Name the blood parasite species.
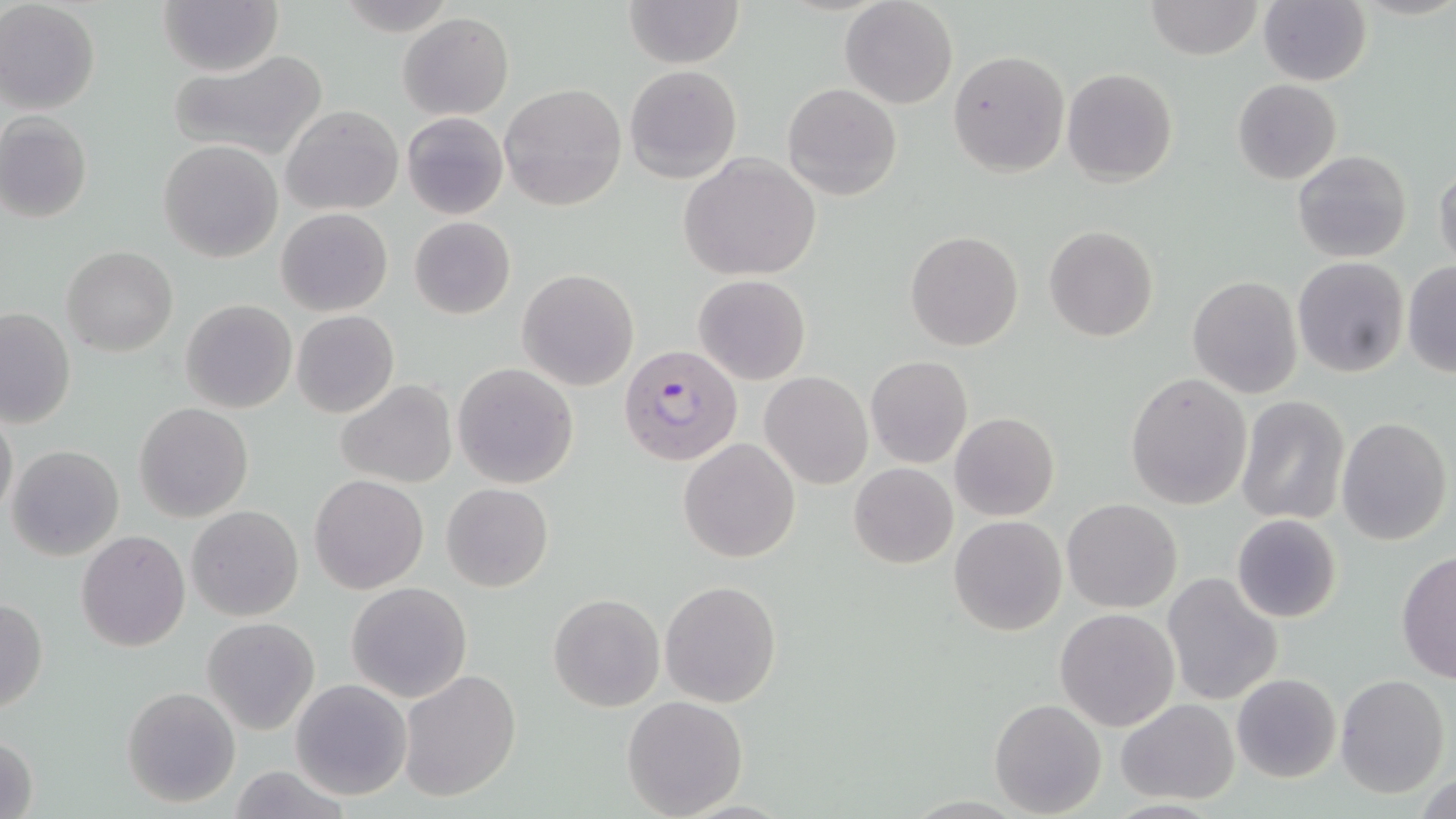
Plasmodium falciparum.

Summary:
  - Coordinate format: approximate bounding boxes as (x1,y1)-(x2,y2) corner pairs in pixels
  - Uninfected red blood cell locations: (0,0)-(101,115), (621,0)-(744,68), (1145,0)-(1263,59), (1260,0)-(1372,87), (158,1)-(284,75), (840,1)-(958,109), (399,12)-(513,121), (166,48)-(328,163), (948,51)-(1069,177), (625,65)-(741,183), (1062,68)-(1179,186), (1232,79)-(1343,185), (782,82)-(902,200), (499,83)-(627,212), (282,105)-(403,215), (400,111)-(509,221), (0,112)-(93,223), (158,139)-(284,263), (1293,149)-(1412,262), (680,154)-(823,281), (1434,166)-(1456,272), (276,208)-(394,315), (409,216)-(515,319), (1044,226)-(1158,343), (905,230)-(1025,352), (62,247)-(178,356), (1293,257)-(1410,377), (1402,261)-(1455,377), (517,267)-(639,392), (693,273)-(811,385), (1188,275)-(1303,398), (180,299)-(296,414), (0,307)-(75,428), (290,310)-(400,419), (865,356)-(974,469), (452,363)-(579,487), (761,371)-(873,489), (1125,371)-(1253,510), (334,379)-(457,489), (1236,396)-(1349,526), (133,402)-(254,521), (1,406)-(19,523), (949,412)-(1060,522), (1336,415)-(1452,545), (678,438)-(800,562), (7,445)-(125,562), (848,463)-(958,569), (310,475)-(429,593), (441,482)-(553,592), (1062,498)-(1182,614), (187,506)-(304,621), (949,515)-(1068,637), (1230,515)-(1343,623), (76,529)-(190,652), (1396,552)-(1456,683), (1161,573)-(1285,707), (660,579)-(782,706), (345,581)-(473,702), (548,593)-(664,711), (0,597)-(48,716), (1054,608)-(1180,731), (201,617)-(320,734), (399,669)-(523,803), (1231,673)-(1342,784), (1336,673)-(1450,796), (290,679)-(411,800), (121,685)-(241,808), (621,695)-(749,818), (990,699)-(1107,817), (1115,700)-(1241,802), (1,733)-(40,819)
  - Plasmodium falciparum-infected red blood cell locations: (619,342)-(744,466)
  - Stain: May-Grünwald-Giemsa
  - Field of view: single
  - Preparation: thin blood smear
  - Modality: optical microscopy
  - Image size: 1456×819 pixels
  - Magnification: 1000x